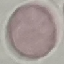
malaria status = uninfected
image type = cell patch, automatically extracted from a larger field of view and resized to 64 × 64 pixels
capture = smartphone through the microscope eyepiece
preparation = thin blood film
stain = Giemsa